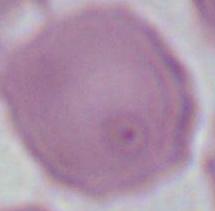
{
  "magnification": "1000x",
  "modality": "photomicrograph",
  "identification": "red blood cell"
}